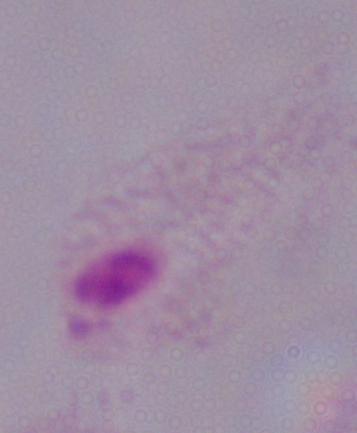

Summary:
  - Modality: photomicrograph
  - Magnification: 1000x
  - Identification: trichomonad